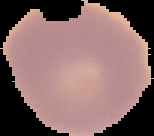
image_size: 154×136 pixels
image_type: segmented cell region on a black background
result: no malaria parasites seen
preparation: thin blood smear